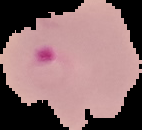
Summary:
  - Preparation: thin blood film
  - Malaria status: parasitized
  - Image size: 142×130 pixels
  - Image type: segmented cell region with the area outside set to black